Identify the preparation type.
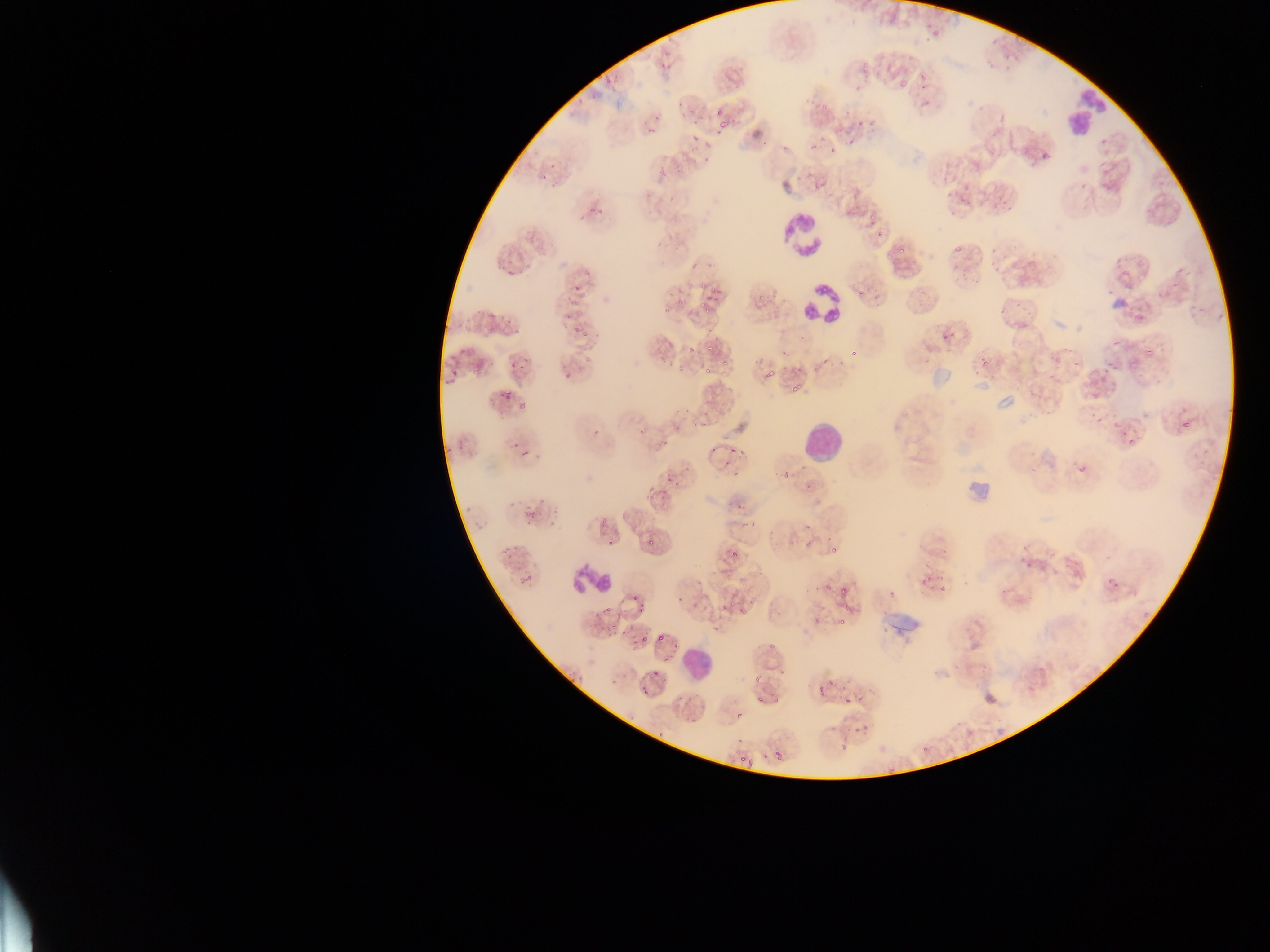
Thin blood smear.

Approximate bounding boxes as [left, top, right, bottom] in pixels. Leukocyte locations: [1063, 87, 1110, 133], [779, 214, 824, 259], [803, 285, 844, 324], [1110, 296, 1126, 313], [803, 423, 845, 464], [568, 558, 612, 602], [682, 644, 716, 681]. Malaria parasite locations: [922, 98, 927, 107], [716, 110, 724, 114], [718, 122, 726, 129], [648, 127, 656, 134], [761, 141, 769, 147], [782, 146, 792, 149], [703, 157, 710, 166], [597, 208, 605, 214], [877, 229, 882, 237], [954, 244, 962, 253], [899, 246, 904, 254], [690, 260, 701, 270], [711, 285, 714, 293], [857, 288, 864, 298], [575, 325, 578, 336], [951, 329, 956, 340], [1145, 345, 1153, 356], [849, 349, 857, 356], [1107, 360, 1113, 368], [677, 362, 682, 371], [705, 365, 712, 373], [471, 366, 479, 375], [766, 368, 774, 379], [794, 382, 801, 392], [518, 403, 526, 411], [1096, 417, 1104, 423], [1182, 420, 1192, 429], [1116, 422, 1122, 430], [592, 430, 600, 434], [1129, 437, 1135, 447], [522, 452, 530, 458], [1079, 465, 1088, 474], [733, 469, 738, 478], [783, 474, 791, 480], [675, 480, 683, 485], [646, 486, 659, 495], [803, 522, 811, 529], [607, 539, 615, 546], [805, 540, 812, 550], [943, 548, 949, 559], [1112, 582, 1120, 589], [1001, 586, 1009, 594], [839, 590, 847, 595], [730, 601, 735, 609], [723, 602, 727, 610], [605, 603, 611, 611], [839, 616, 845, 624], [716, 623, 720, 631], [641, 633, 647, 641], [658, 633, 666, 642], [769, 641, 774, 650], [782, 666, 786, 675], [654, 669, 658, 677], [827, 677, 834, 685], [819, 685, 825, 699], [643, 690, 651, 695], [757, 695, 762, 703], [736, 711, 743, 721], [691, 717, 697, 725], [853, 724, 862, 735], [657, 731, 668, 740], [840, 741, 848, 750], [776, 748, 783, 761], [749, 756, 756, 766] | approximate [x, y] pixel centers of objects too small to bound: [595, 98], [680, 105], [691, 111], [657, 118], [695, 122], [861, 123], [694, 140], [850, 143], [552, 165], [871, 217], [890, 255], [587, 272], [577, 289], [761, 296], [717, 300], [680, 302], [702, 304], [706, 310], [510, 322], [517, 331], [586, 335], [945, 338], [671, 346], [710, 347], [692, 350], [784, 354], [983, 360], [825, 361], [513, 365], [454, 372], [568, 375], [793, 389], [502, 396], [508, 399], [1124, 433], [665, 442], [515, 446], [712, 450], [733, 450], [742, 452], [669, 479], [542, 499], [512, 505], [739, 506], [528, 513], [534, 517], [604, 521], [752, 524], [651, 542], [515, 546], [1025, 548], [507, 549], [833, 550], [734, 552], [510, 557], [1028, 566], [529, 577], [923, 580], [522, 581], [828, 589], [942, 590], [894, 594], [634, 599], [680, 600], [641, 609], [741, 611], [613, 628], [623, 634], [675, 646], [668, 659], [757, 678], [861, 698], [775, 701], [847, 701], [739, 741], [925, 749], [766, 755], [742, 759]. Artifact (stain precipitate or debris) locations: [1052, 316, 1069, 331], [937, 361, 961, 393], [975, 379, 990, 394], [996, 392, 1017, 412], [968, 469, 995, 504], [880, 603, 923, 638]. Photographed through a microscope with a mobile-phone camera. One field of view. Collected in Ghana. Image is 1270×952 pixels.